Give the extent of all Plasmodium parasites.
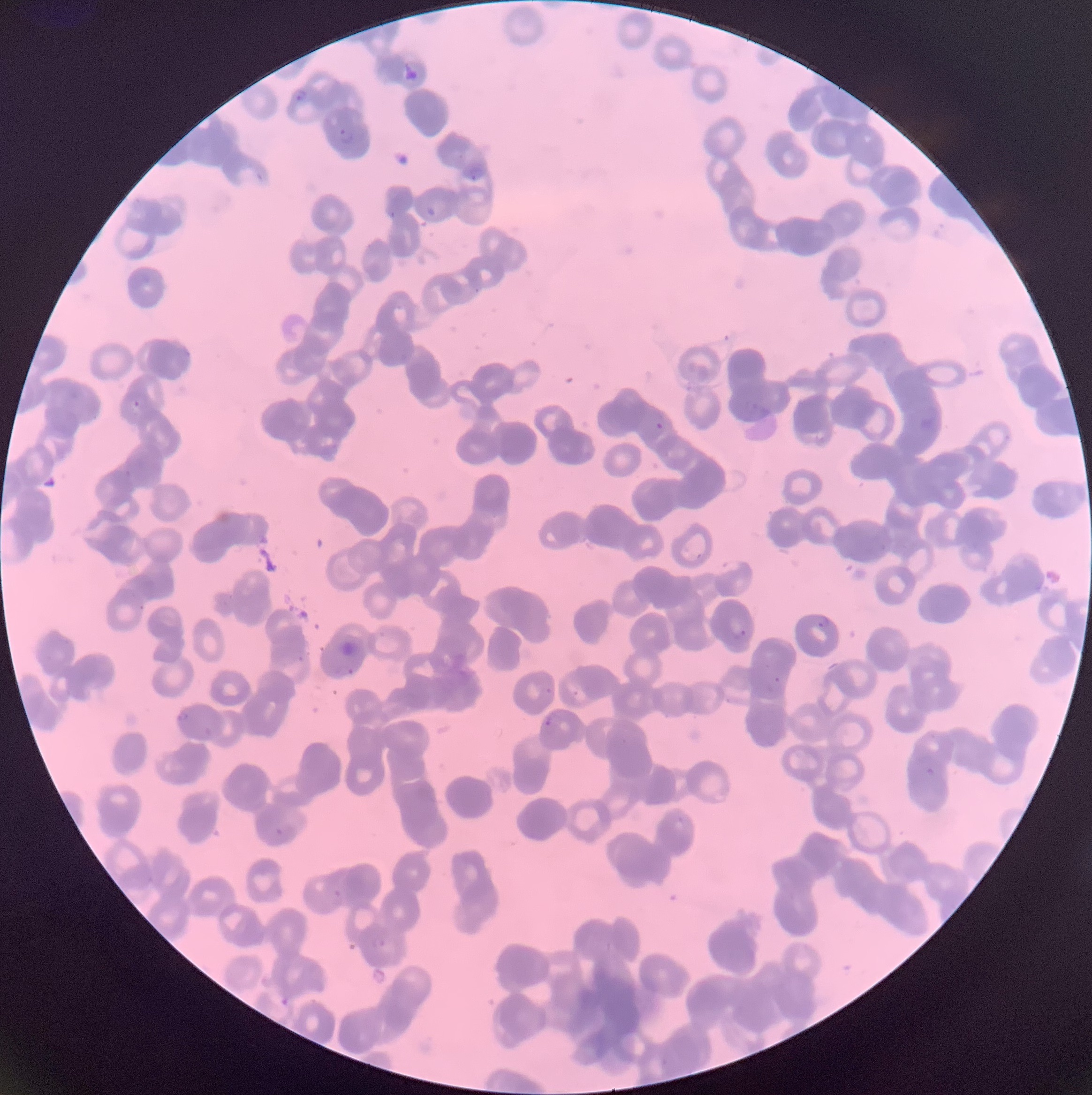
Approximate bounding boxes as (x1, y1, x2, y2) in pixels.
Plasmodium parasites: (402, 63, 420, 82), (296, 89, 307, 102), (338, 127, 354, 145), (467, 165, 486, 181), (425, 206, 438, 216), (132, 399, 142, 407), (653, 422, 665, 430), (817, 615, 831, 629), (728, 619, 749, 639), (334, 665, 355, 677), (545, 687, 553, 696), (572, 689, 579, 697), (177, 711, 193, 723), (544, 712, 564, 729), (926, 767, 937, 776), (274, 828, 287, 837), (333, 889, 345, 899), (370, 936, 386, 948), (278, 995, 291, 1007).
Plasmodium parasites too small for a box (approximate centers as (x, y) in pixels): (777, 679).

preparation = thin blood film
modality = optical microscopy
image size = 1092×1095 pixels
red blood cell morphology = rouleaux formation